Report the malaria status of this cell.
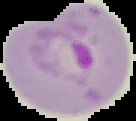

It is parasitized.

Summary:
  - Image type: segmented cell region on a black background
  - Image size: 136×121 pixels
  - Preparation: thin blood smear